Describe the morphology of the erythrocytes.
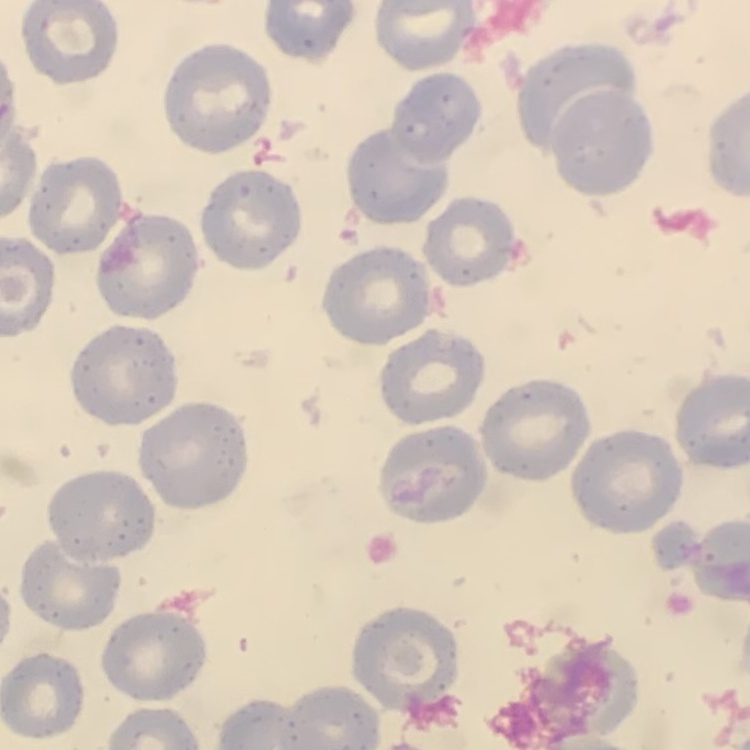
They show no rouleaux formation.

Summary:
  - Stain: Field's or Giemsa
  - Preparation: thin blood film
  - Image type: square crop of a larger photomicrograph